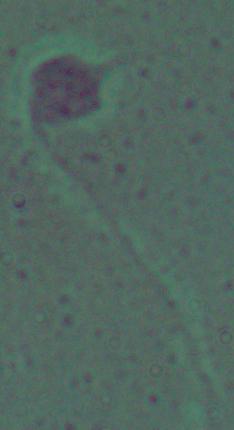
identification = Leishmania
modality = micrograph
magnification = 1000x